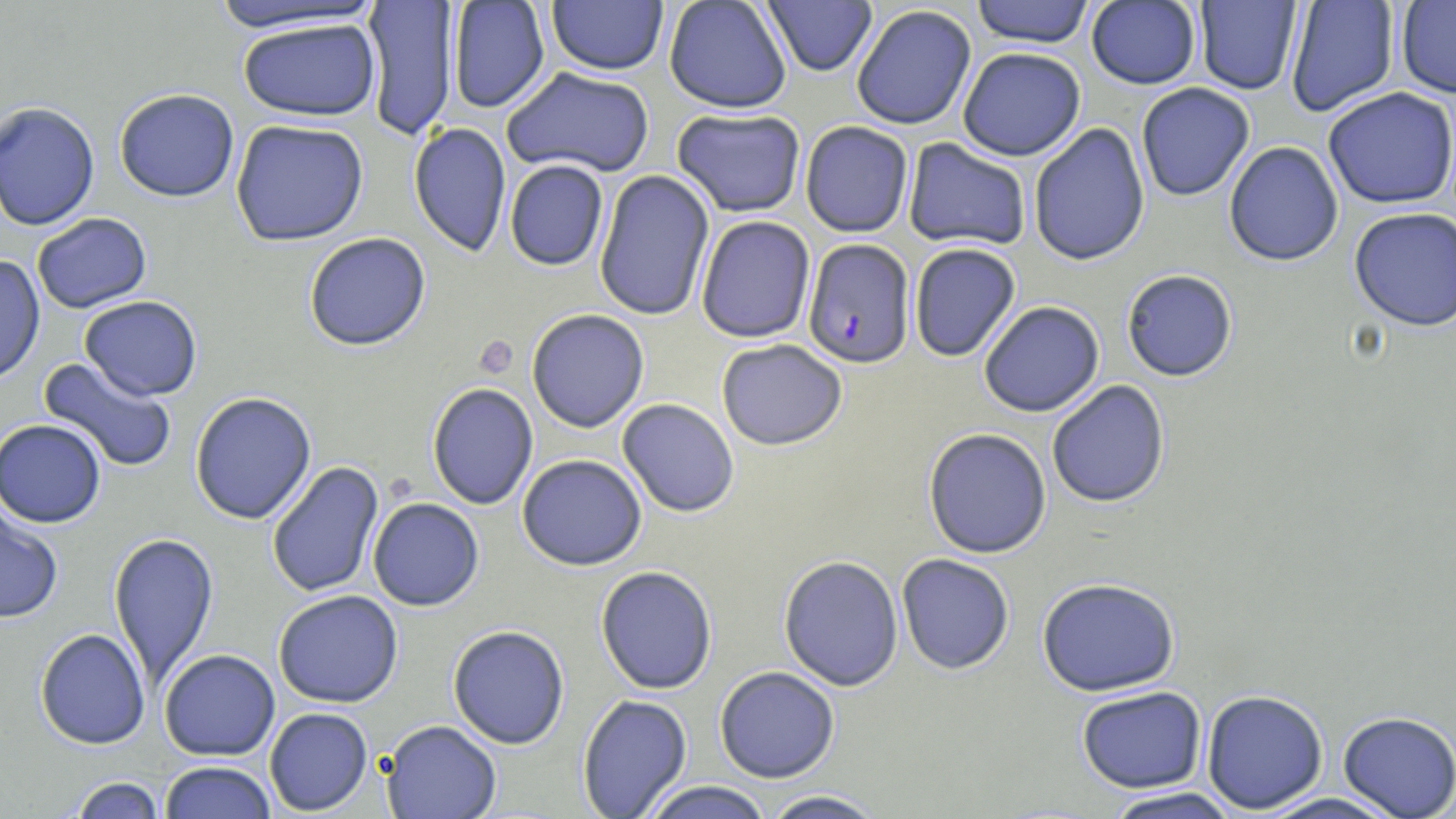
Approximate bounding boxes as [x1, y1, x2, y2] in pixels. Uninfected red blood cell locations: [447, 0, 550, 114], [663, 0, 792, 113], [970, 0, 1095, 47], [206, 1, 387, 35], [361, 1, 459, 141], [546, 1, 669, 76], [762, 1, 877, 76], [1086, 1, 1201, 89], [1194, 1, 1302, 95], [1285, 1, 1400, 117], [1396, 1, 1456, 98], [851, 4, 977, 131], [237, 17, 380, 121], [957, 47, 1086, 160], [501, 66, 656, 178], [1136, 83, 1255, 201], [1323, 87, 1456, 209], [114, 88, 239, 202], [0, 101, 100, 230], [671, 107, 807, 217], [230, 118, 369, 246], [800, 120, 914, 238], [407, 122, 512, 257], [1028, 123, 1150, 266], [902, 138, 1032, 251], [1224, 141, 1344, 267], [504, 159, 609, 271], [593, 169, 715, 321], [1348, 207, 1456, 332], [31, 213, 152, 313], [695, 215, 816, 343], [304, 232, 431, 351], [909, 243, 1022, 362], [0, 255, 45, 385], [1121, 269, 1238, 381], [80, 295, 202, 400], [978, 301, 1105, 417], [526, 309, 650, 433], [716, 338, 847, 451], [38, 357, 178, 474], [1046, 380, 1170, 508], [426, 382, 539, 510], [190, 391, 316, 524], [617, 398, 740, 517], [0, 418, 106, 528], [923, 427, 1052, 559], [517, 454, 647, 571], [266, 461, 384, 599], [367, 497, 484, 611], [0, 503, 64, 624], [108, 532, 219, 688], [896, 553, 1015, 674], [778, 555, 904, 691], [595, 565, 717, 694], [1037, 577, 1181, 696], [273, 590, 404, 708], [447, 625, 570, 749], [35, 627, 151, 750], [159, 648, 280, 760], [714, 666, 840, 783], [1076, 686, 1207, 793], [1201, 689, 1329, 813], [577, 694, 692, 818], [264, 707, 373, 815], [1338, 711, 1456, 819], [380, 720, 502, 819], [159, 761, 277, 819], [68, 776, 165, 819], [639, 781, 776, 819], [1101, 787, 1242, 819], [759, 789, 889, 818], [1253, 792, 1407, 819]. Platelet locations: [475, 336, 519, 378]. Plasmodium falciparum-infected red blood cell locations: [803, 238, 915, 369]. Slide-level diagnosis: Plasmodium falciparum. May-Grünwald-Giemsa stain. Image is 1456×819 pixels. Thin blood smear. Optical microscopy. Single field of view. 1000x magnification.